Name the cell type shown.
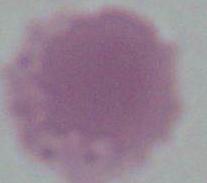
This is an erythrocyte.

Summary:
  - Modality: photomicrograph
  - Magnification: 1000x